State the preparation type.
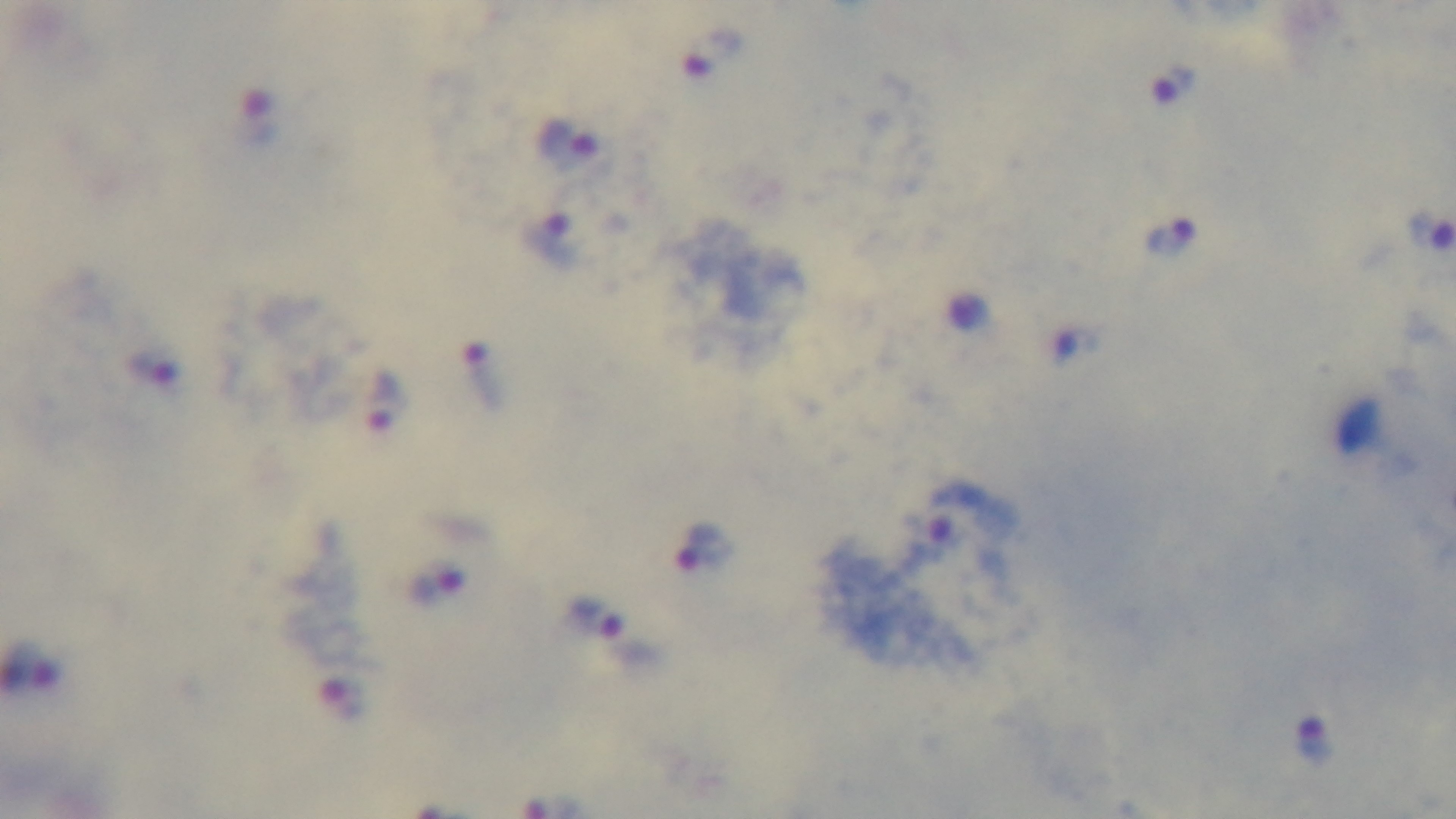
Thick.

Oil-immersion objective, 100x. Malaria status: positive. One field from the slide. Giemsa stain. Mounted 4K digital camera. Light microscopy.